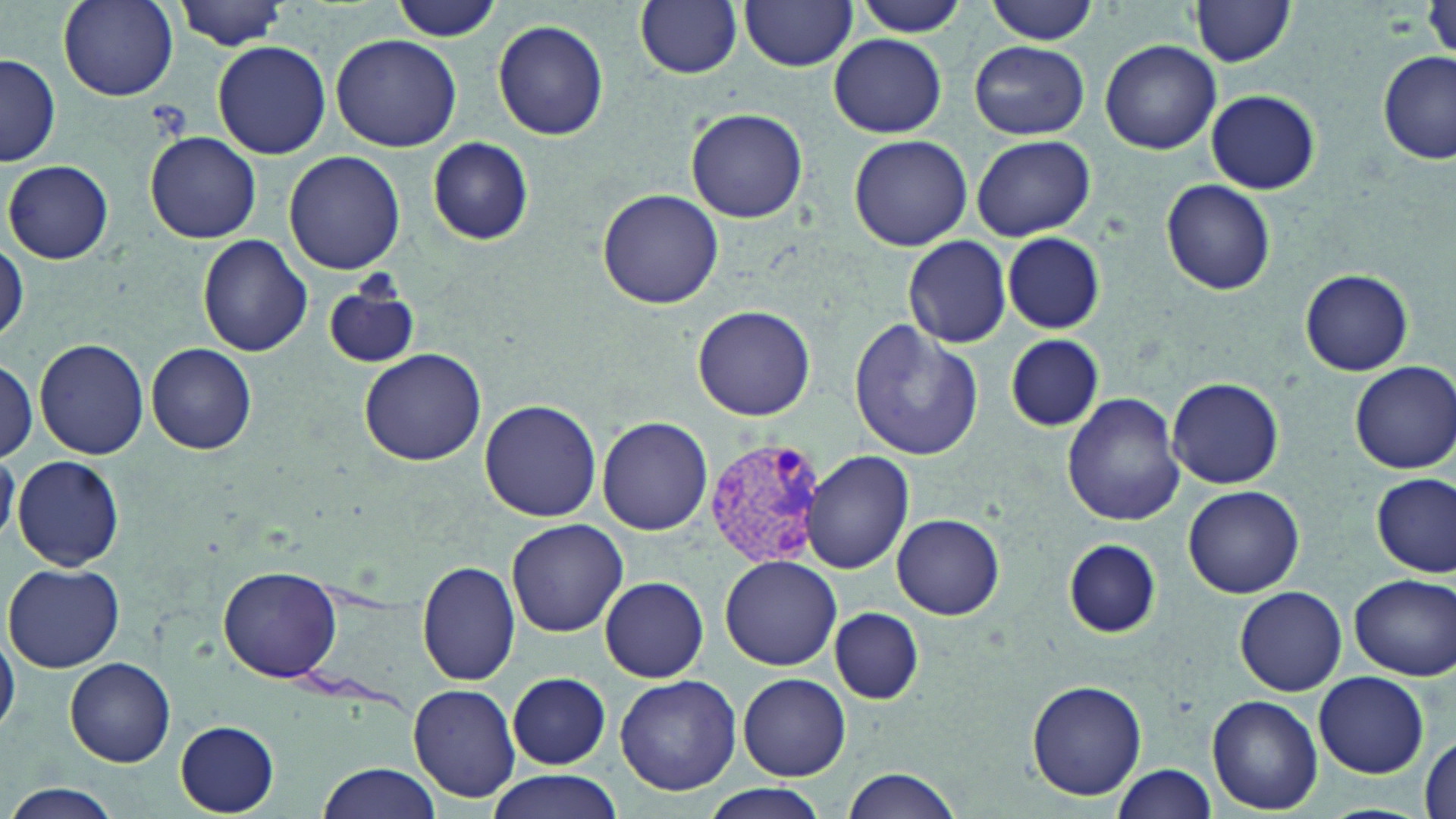

slide-level diagnosis = Plasmodium vivax
modality = optical microscopy
uninfected red blood cell locations = approximate bounding boxes as [x1, y1, x2, y2] in pixels: [58, 0, 177, 102], [392, 0, 498, 45], [635, 0, 743, 78], [741, 0, 856, 72], [984, 0, 1100, 44], [175, 1, 294, 50], [850, 1, 971, 36], [1190, 2, 1295, 67], [492, 20, 609, 140], [331, 34, 462, 153], [828, 34, 947, 137], [1099, 38, 1222, 154], [227, 39, 439, 161], [212, 41, 331, 159], [969, 41, 1088, 139], [1377, 51, 1454, 164], [1, 53, 62, 166], [1206, 89, 1320, 194], [686, 107, 810, 223], [145, 132, 262, 242], [849, 135, 972, 251], [971, 135, 1095, 241], [428, 137, 533, 245], [283, 152, 404, 275], [5, 161, 114, 265], [1159, 180, 1276, 294], [597, 189, 725, 311], [1003, 233, 1104, 334], [902, 234, 1012, 348], [196, 235, 312, 357], [0, 241, 27, 345], [1299, 269, 1412, 375], [323, 280, 422, 369], [693, 304, 816, 421], [848, 321, 985, 461], [1003, 335, 1106, 433], [34, 338, 152, 460], [147, 343, 257, 453], [359, 349, 486, 464], [0, 361, 37, 463], [1351, 362, 1456, 473], [1167, 377, 1284, 489], [1062, 393, 1184, 526], [480, 399, 601, 522], [597, 416, 713, 535], [804, 451, 914, 575], [12, 454, 124, 570], [1371, 473, 1454, 577], [1183, 485, 1305, 598], [892, 513, 1004, 620], [506, 519, 628, 638], [1063, 540, 1160, 638], [720, 556, 841, 670], [417, 561, 520, 685], [5, 563, 125, 672], [217, 563, 342, 681], [1349, 574, 1455, 680], [600, 576, 710, 682], [1233, 585, 1346, 695], [829, 607, 923, 703], [0, 633, 20, 735], [65, 657, 177, 766], [507, 672, 610, 768], [1314, 672, 1428, 777], [738, 674, 850, 780], [614, 675, 741, 795], [1027, 678, 1147, 801], [408, 685, 519, 800], [1207, 695, 1323, 813], [175, 720, 280, 815], [1418, 734, 1454, 819], [314, 762, 441, 819], [1112, 762, 1218, 818], [485, 770, 623, 819], [841, 770, 963, 819], [3, 782, 125, 819], [700, 785, 835, 819]
Plasmodium vivax-infected red blood cell locations = approximate bounding boxes as [x1, y1, x2, y2] in pixels: [704, 439, 824, 569]
preparation = thin blood smear
stain = May-Grünwald-Giemsa
magnification = 1000x
field of view = one of a larger specimen
image size = 1456×819 pixels